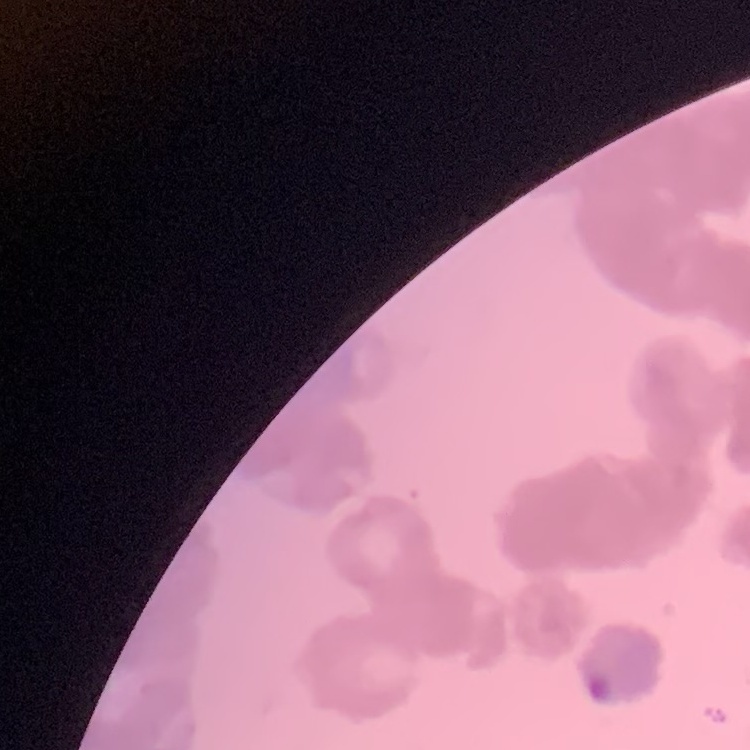

red_blood_cell_morphology: rouleaux formation
stain: Field's or Giemsa
image_type: square crop of a larger photomicrograph
preparation: thin blood smear